Outline each blood parasite and name the species.
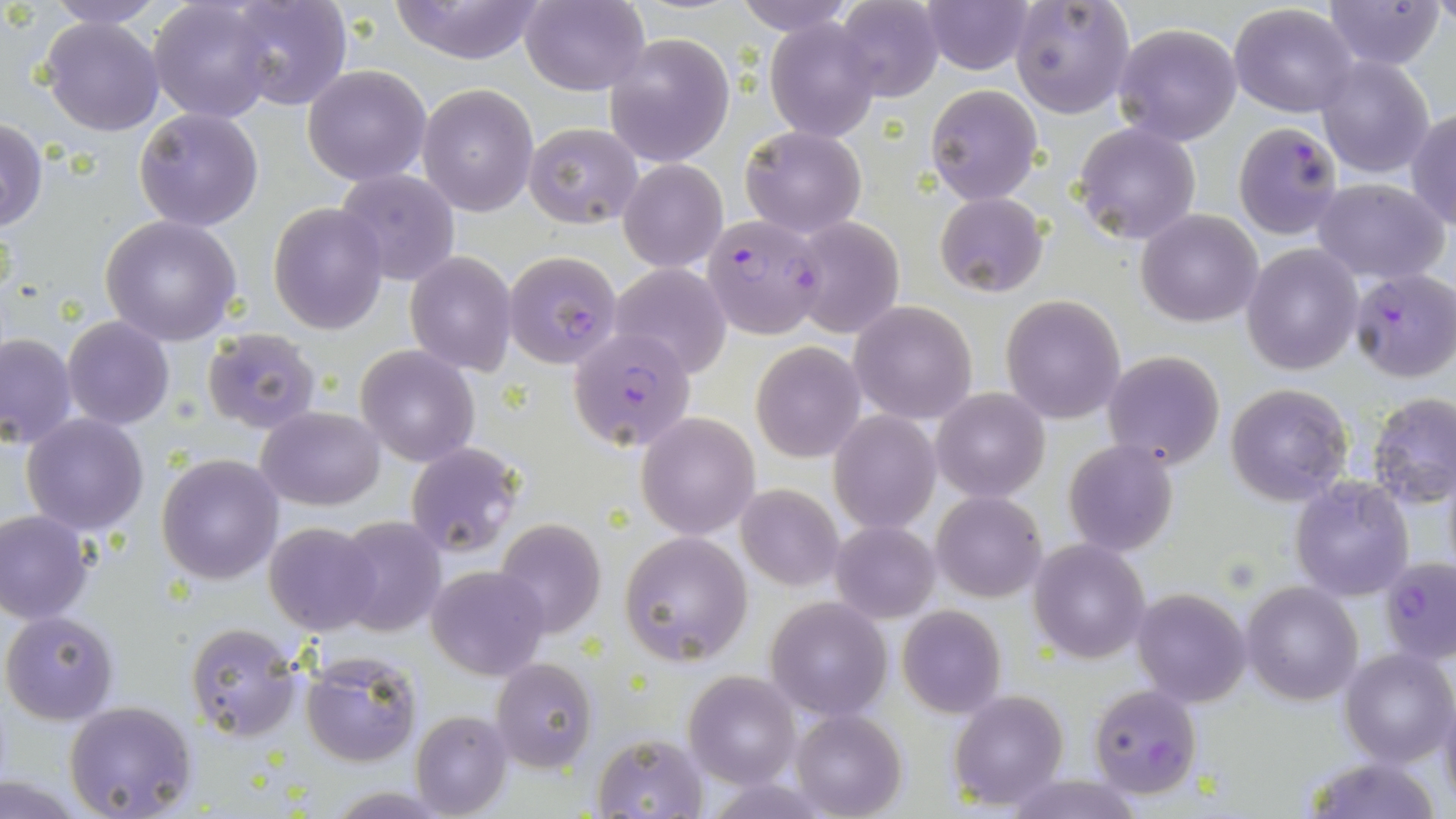
Approximate bounding boxes as [x1, y1, x2, y2] in pixels.
Plasmodium falciparum-infected red blood cells: [1233, 120, 1345, 239], [701, 214, 825, 339], [504, 250, 625, 371], [1348, 268, 1455, 382], [567, 328, 696, 452], [1382, 557, 1456, 663], [1088, 684, 1203, 798].
No Plasmodium ovale, Plasmodium malariae, Plasmodium vivax, Babesia divergens, or Trypanosoma brucei observed.

Uninfected red blood cell locations: [42, 0, 169, 29], [149, 0, 277, 121], [222, 0, 353, 112], [385, 0, 550, 64], [521, 0, 649, 95], [737, 0, 853, 35], [919, 0, 1036, 76], [1011, 0, 1135, 119], [1321, 0, 1447, 71], [834, 1, 943, 102], [1229, 3, 1360, 117], [40, 16, 163, 135], [766, 19, 880, 142], [1112, 21, 1244, 147], [604, 34, 735, 167], [1315, 55, 1437, 177], [303, 64, 432, 185], [417, 82, 540, 216], [926, 83, 1042, 204], [135, 107, 263, 231], [1408, 107, 1456, 229], [1, 118, 48, 233], [524, 122, 642, 228], [1074, 122, 1200, 245], [740, 124, 866, 238], [619, 156, 728, 272], [336, 170, 459, 285], [1311, 177, 1449, 282], [933, 192, 1049, 297], [269, 202, 388, 334], [1137, 209, 1264, 327], [99, 216, 242, 345], [789, 217, 904, 337], [1240, 244, 1362, 375], [405, 249, 517, 377], [607, 263, 732, 378], [1001, 295, 1126, 423], [850, 300, 978, 423], [62, 317, 175, 428], [200, 328, 323, 435], [0, 332, 78, 449], [751, 342, 865, 462], [356, 346, 479, 466], [1102, 352, 1225, 469], [1225, 384, 1353, 505], [932, 388, 1050, 501], [1367, 392, 1456, 509], [256, 406, 385, 511], [831, 410, 940, 532], [637, 412, 759, 539], [22, 413, 148, 535], [1063, 440, 1179, 556], [405, 441, 523, 558], [157, 453, 283, 584], [1291, 477, 1414, 601], [736, 483, 844, 592], [932, 491, 1047, 602], [1, 510, 93, 623], [334, 516, 444, 638], [494, 518, 607, 638], [830, 520, 942, 623], [263, 521, 380, 635], [618, 531, 753, 665], [1029, 540, 1148, 663], [426, 565, 549, 679], [1243, 581, 1363, 704], [1133, 588, 1251, 708], [766, 598, 892, 721], [898, 605, 1006, 718], [2, 610, 121, 724], [185, 622, 302, 741], [1338, 646, 1454, 768], [299, 653, 420, 766], [491, 657, 597, 771], [683, 671, 800, 787], [950, 689, 1069, 812], [1441, 690, 1456, 816], [64, 701, 197, 818], [791, 708, 906, 818], [410, 712, 512, 818], [591, 732, 709, 818], [1299, 756, 1448, 818], [1004, 774, 1145, 818]. Slide-level diagnosis: Plasmodium falciparum. May-Grünwald-Giemsa stain. Captured at 1000x magnification. Thin blood film. One field of a larger specimen. Light microscopy. Image is 1456×819 pixels.